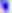
magnification = 400x
identification = Toxoplasma gondii
modality = photomicrograph